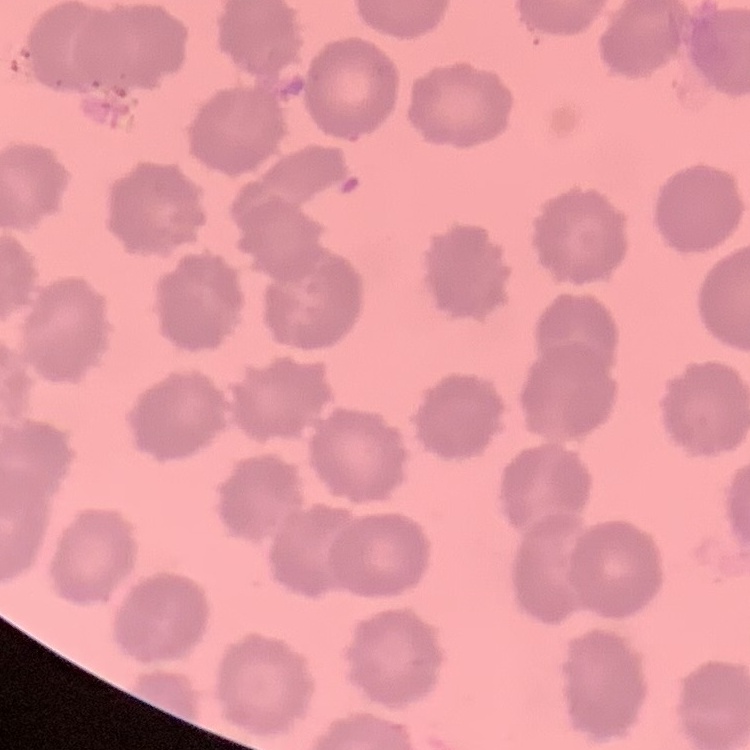
red blood cell morphology = no rouleaux formation
stain = Field's or Giemsa
preparation = thin blood film
image type = square crop of a larger photomicrograph